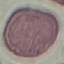
Result: no malaria parasites seen. Acquired by smartphone through the microscope eyepiece. Giemsa-stained preparation. Cell patch, automatically extracted from a larger field of view and resized to 64 × 64 pixels. Thin smear of blood.